State which parasite is depicted.
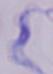
A trypanosome.

magnification: 1000x
modality: micrograph